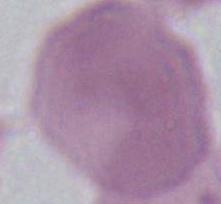
Summary:
  - Modality: micrograph
  - Identification: erythrocyte
  - Magnification: 1000x